Report the malaria status of this cell.
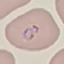
It is parasitized.

Automatically extracted cell patch, resized to 64 × 64 pixels. Thin blood smear. Acquired by smartphone through the microscope eyepiece. Giemsa-stained preparation.